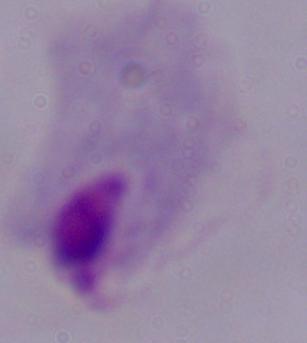
{
  "magnification": "1000x",
  "modality": "photomicrograph",
  "identification": "trichomonad"
}